Identify the cell.
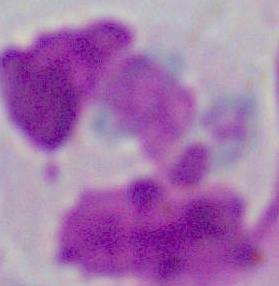
A leukocyte.

Summary:
  - Modality: micrograph
  - Magnification: 1000x